Assess this cell for malaria.
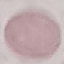

It is uninfected.

Summary:
  - Preparation: thin blood smear
  - Capture: smartphone camera at the microscope eyepiece
  - Stain: Giemsa
  - Image type: automatically extracted cell patch, resized to 64 × 64 pixels